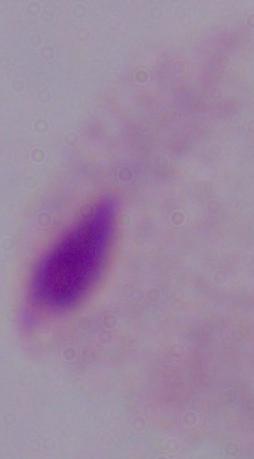
Summary:
  - Modality: micrograph
  - Identification: trichomonad
  - Magnification: 1000x